Assess this cell for malaria.
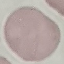

Uninfected.

Summary:
  - Stain: Giemsa
  - Image type: cell patch, automatically extracted from a larger field of view and resized to 64 × 64 pixels
  - Preparation: thin smear
  - Capture: smartphone camera at the microscope eyepiece